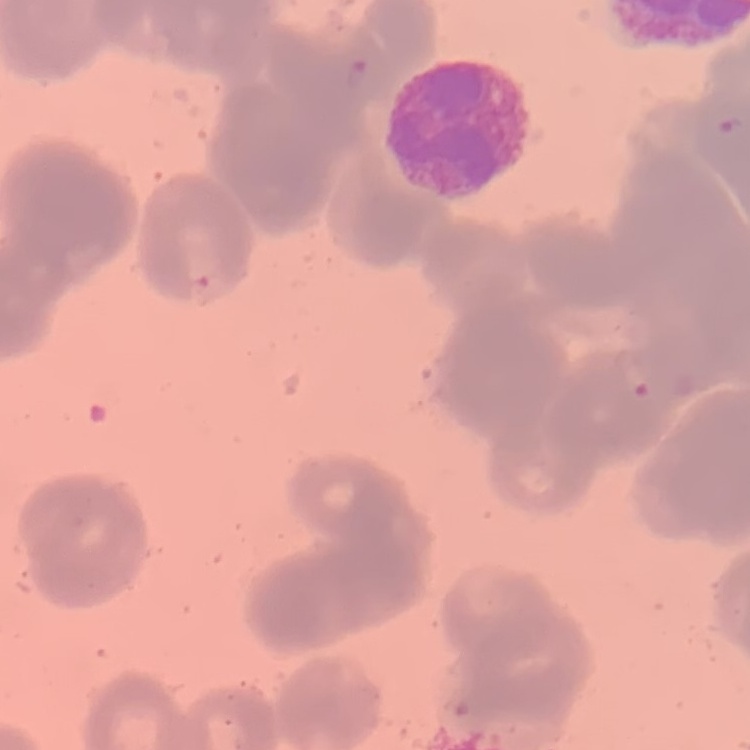

erythrocyte morphology = rouleaux formation
stain = Field's or Giemsa
image type = one tile cut from a larger photomicrograph
preparation = thin blood film